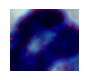
Summary:
  - Magnification: 1000x
  - Modality: micrograph
  - Identification: leukocyte